Name the parasite shown.
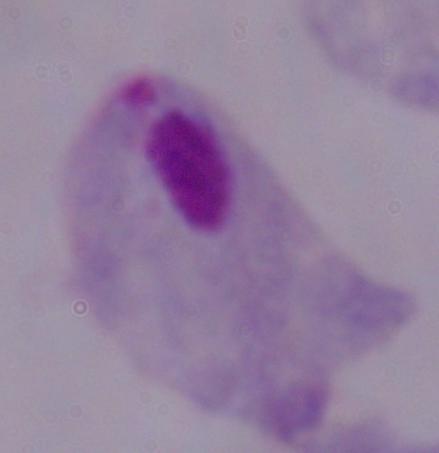

This is a trichomonad.

Summary:
  - Magnification: 1000x
  - Modality: photomicrograph